Comment on the morphology of the erythrocytes.
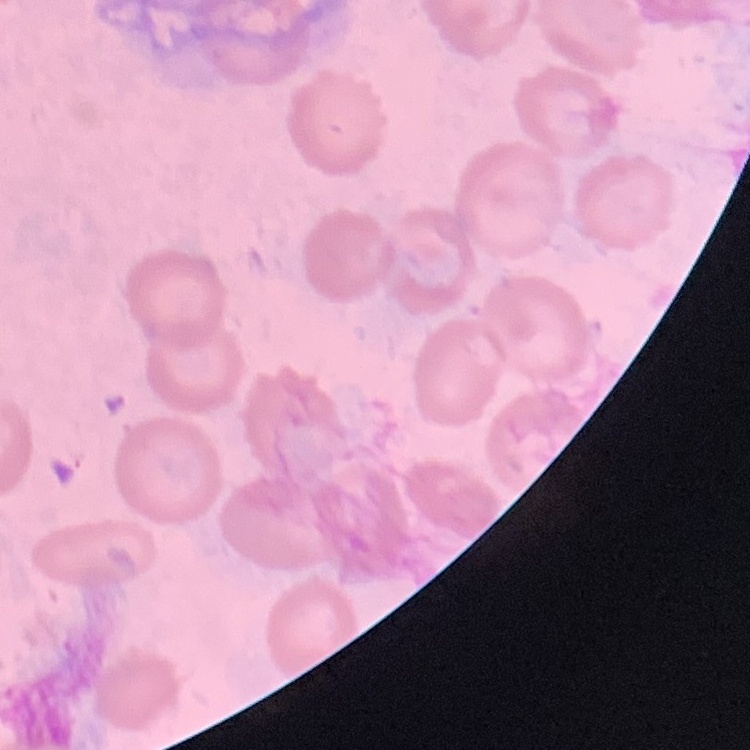
They show no rouleaux formation.

Square crop of a larger photomicrograph. Field's or Giemsa stain. Thin peripheral smear.